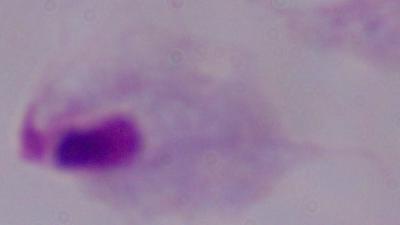

{
  "identification": "trichomonad",
  "magnification": "1000x",
  "modality": "photomicrograph"
}